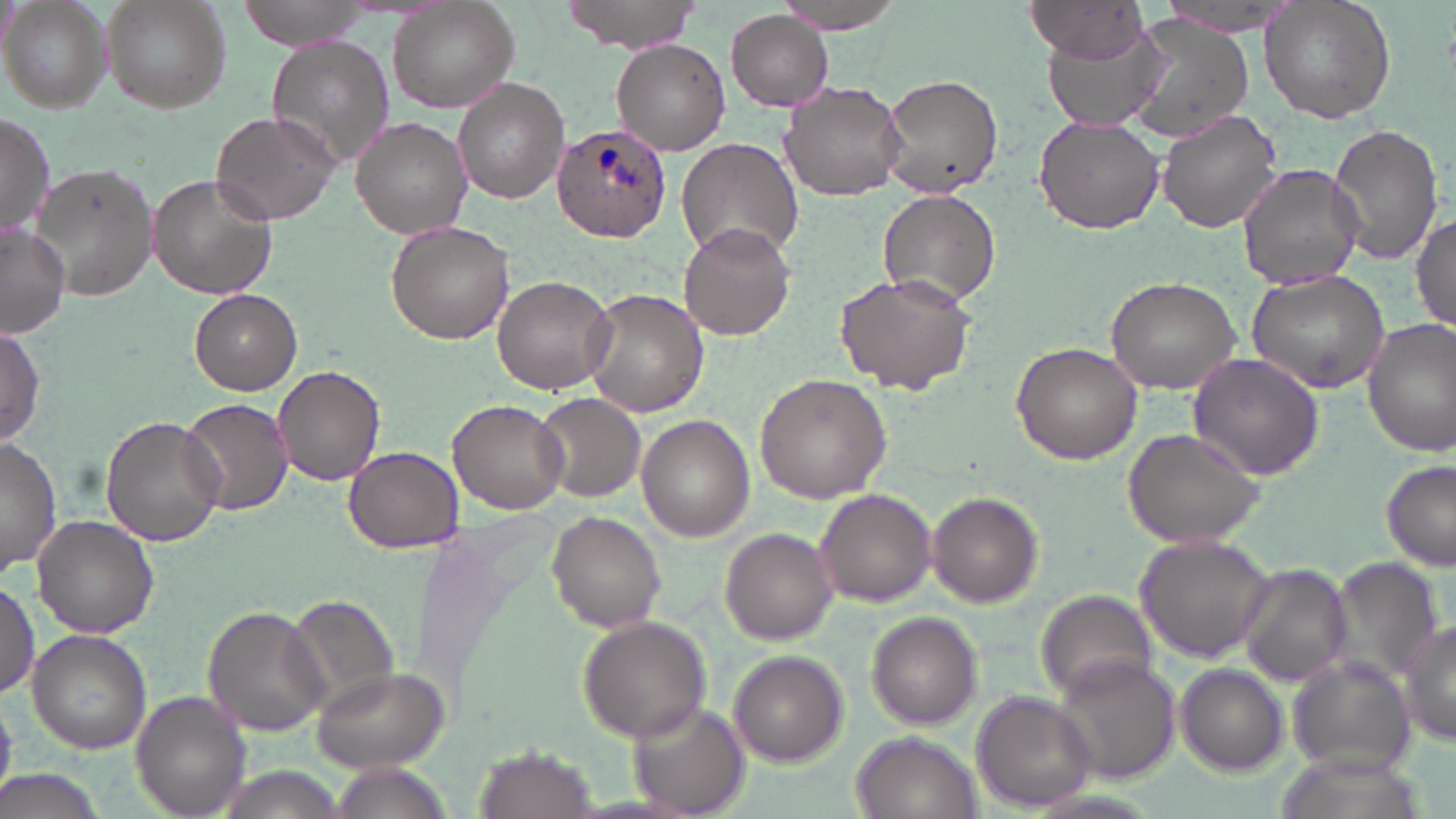

Summary:
  - Coordinate format: approximate bounding boxes as (x1,y1)-(x2,y2) corner pairs in pixels
  - Plasmodium ovale-infected red blood cell locations: (551,122)-(672,242)
  - Uninfected red blood cell locations: (103,0)-(233,112), (236,0)-(374,49), (560,0)-(706,53), (781,0)-(911,32), (1259,0)-(1397,123), (0,1)-(112,113), (388,1)-(520,112), (1024,2)-(1152,60), (726,11)-(834,110), (1125,16)-(1256,138), (1039,26)-(1168,134), (264,35)-(398,171), (610,39)-(730,155), (880,72)-(1004,195), (453,79)-(570,203), (779,81)-(906,202), (1157,109)-(1283,233), (210,110)-(340,225), (0,113)-(55,242), (1034,114)-(1168,238), (351,116)-(473,238), (1328,123)-(1443,265), (675,138)-(803,261), (31,162)-(157,301), (1237,163)-(1364,290), (147,172)-(277,300), (877,189)-(1001,310), (1412,212)-(1456,334), (385,221)-(514,345), (679,221)-(795,342), (0,225)-(70,337), (1246,266)-(1392,394), (832,270)-(977,392), (492,273)-(619,393), (1105,274)-(1247,393), (190,288)-(302,396), (581,288)-(708,418), (1362,318)-(1456,454), (0,325)-(47,448), (1011,341)-(1142,463), (1188,352)-(1324,480), (272,365)-(385,485), (756,373)-(890,503), (534,393)-(646,504), (180,397)-(294,516), (447,398)-(570,515), (100,415)-(225,546), (637,415)-(755,544), (1122,425)-(1266,549), (0,440)-(60,577), (343,446)-(463,553), (1379,458)-(1455,572), (813,489)-(936,607), (928,491)-(1043,607), (548,510)-(667,634), (31,516)-(160,639), (720,528)-(837,644), (1137,534)-(1279,663), (1321,559)-(1444,686), (1236,563)-(1353,686), (0,578)-(40,701), (1034,588)-(1158,702), (283,594)-(404,711), (202,605)-(327,737), (867,612)-(982,729), (576,614)-(713,742), (1396,622)-(1456,748), (25,630)-(151,755), (729,651)-(847,765), (1287,656)-(1418,780), (1052,657)-(1180,784), (1175,662)-(1286,776), (312,667)-(447,771), (972,690)-(1097,810), (131,691)-(251,819), (627,701)-(749,816), (853,732)-(984,819), (473,746)-(595,818), (329,762)-(444,819), (0,769)-(108,819)
  - Slide-level diagnosis: Plasmodium ovale
  - Preparation: thin blood film
  - Modality: optical microscopy
  - Magnification: 1000x
  - Image size: 1456×819 pixels
  - Field of view: single
  - Stain: May-Grünwald-Giemsa